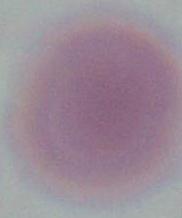

Summary:
  - Modality: photomicrograph
  - Identification: erythrocyte
  - Magnification: 1000x